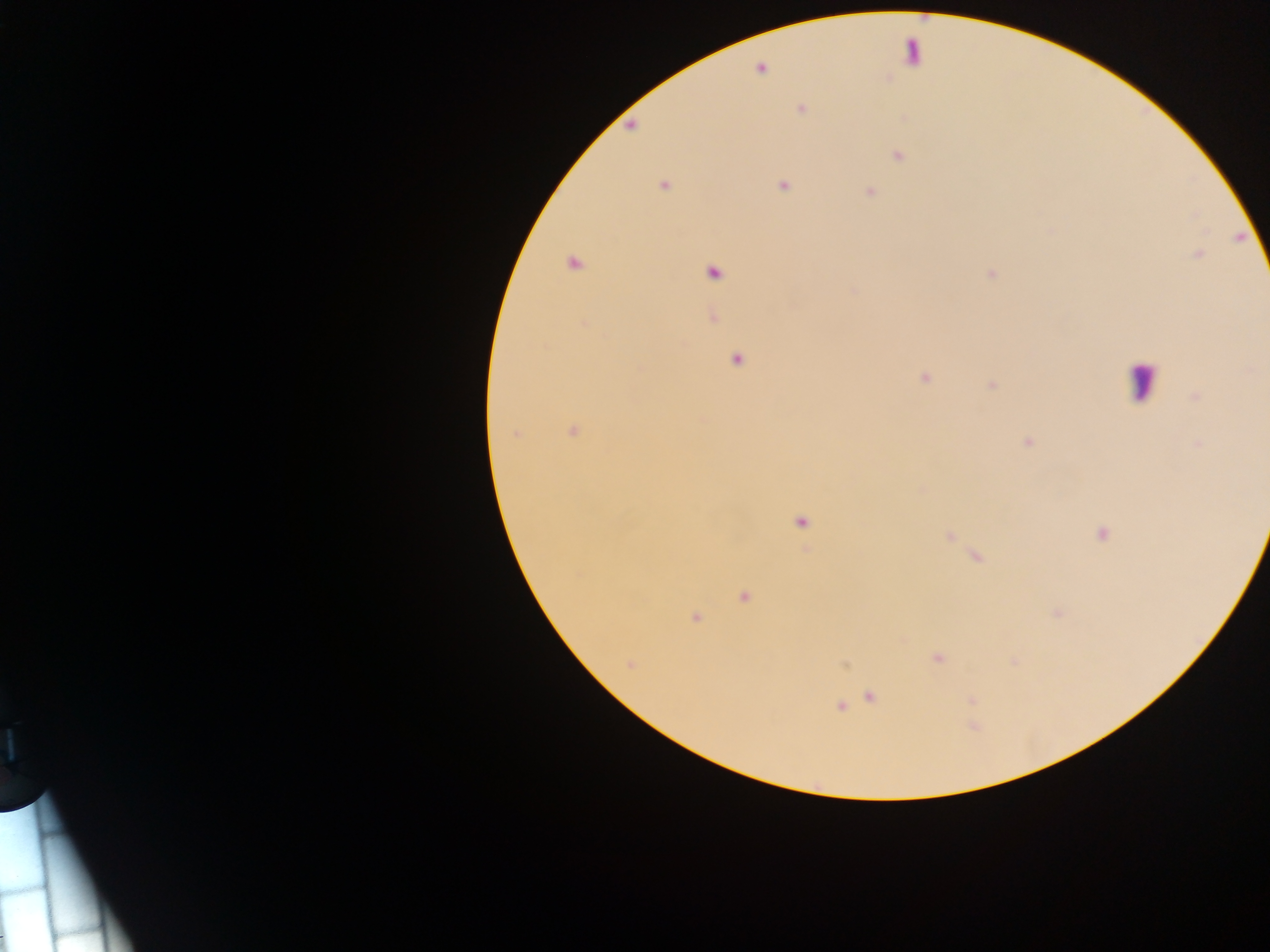
Approximate centers as [x, y] in pixels.
Summary:
  - Leukocyte locations: [912, 54], [1142, 381]
  - Malaria parasite locations: [759, 70], [801, 109], [630, 123], [899, 156], [663, 185], [783, 185], [870, 191], [1199, 255], [573, 264], [990, 273], [714, 274], [853, 291], [583, 323], [737, 360], [924, 377], [991, 385], [1196, 396], [574, 431], [516, 434], [1028, 442], [1198, 444], [801, 522], [1102, 534], [947, 536], [744, 597], [1057, 613], [695, 618], [937, 659], [630, 665], [871, 698], [841, 706]
  - Country: Ghana
  - Image size: 1270×952 pixels
  - Capture: mobile-phone photograph through a microscope
  - Field of view: single
  - Preparation: thick blood film